Locate every malaria parasite.
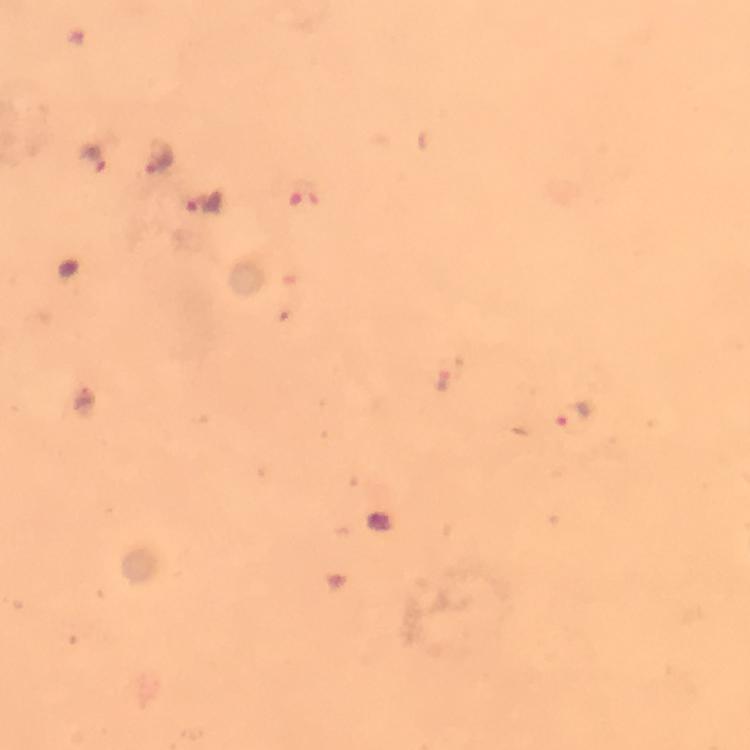

Approximate centers as (x, y) in pixels.
Malaria parasites: (91, 158), (157, 158), (203, 203), (573, 415).

Summary:
  - Preparation: thick blood smear
  - Context: from a diagnostic examination for malaria
  - Cropped from: one field of view
  - Immersion oil: applied
  - Image size: 750×750 pixels
  - Stain: Giemsa
  - Magnification: 100x
  - Capture: smartphone mounted on the microscope